Outline each uninfected red blood cell.
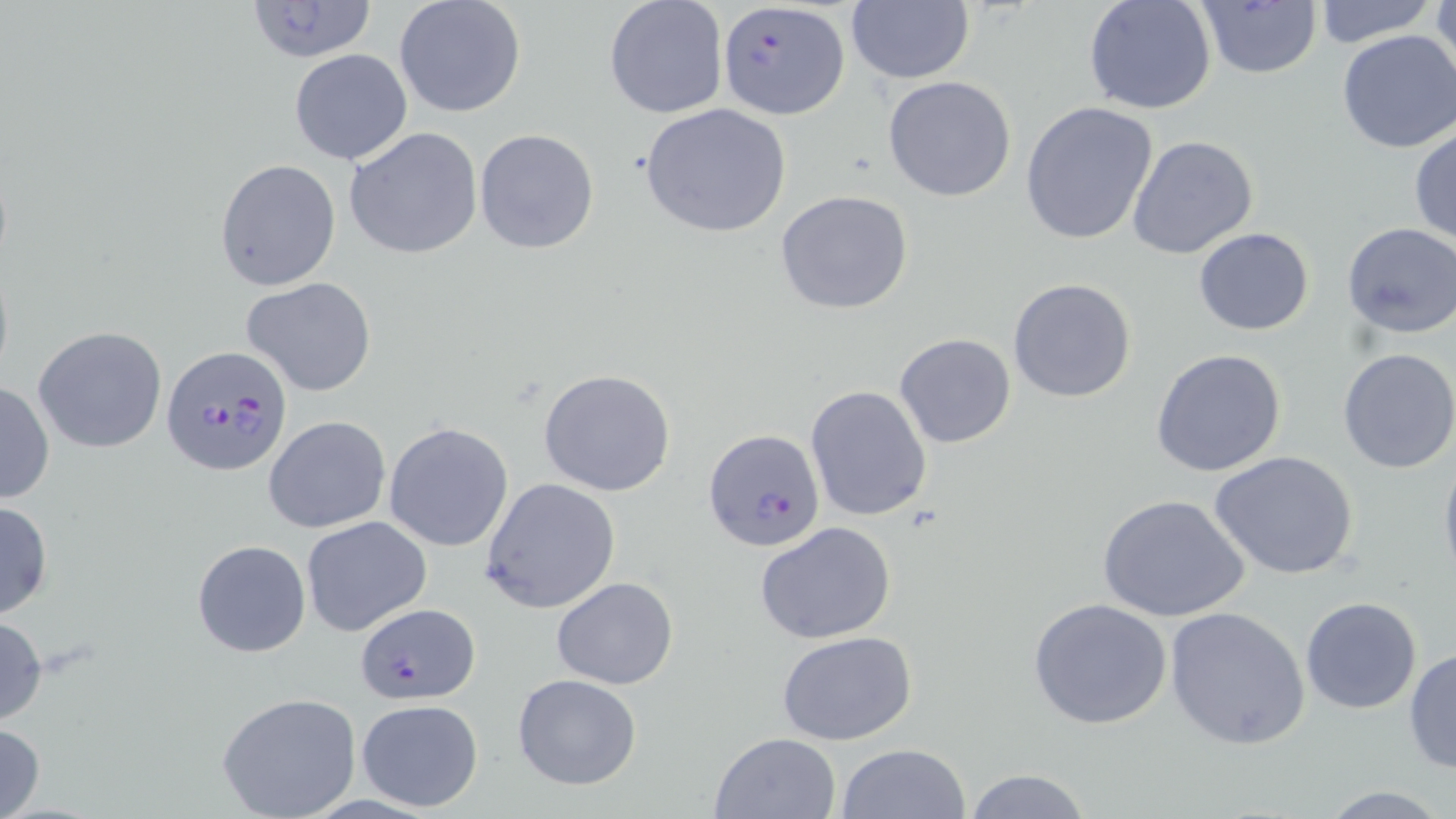
Approximate bounding boxes as (x1,y1)-(x2,y2) corner pairs in pixels.
Uninfected red blood cells: (393,0)-(527,120), (603,0)-(728,120), (846,0)-(974,86), (1083,0)-(1218,116), (1431,0)-(1456,87), (1312,1)-(1437,48), (1193,2)-(1323,80), (1335,29)-(1456,153), (289,48)-(413,165), (882,76)-(1016,203), (1020,101)-(1160,247), (639,104)-(791,237), (1409,122)-(1456,245), (344,126)-(482,260), (475,128)-(600,255), (1128,135)-(1259,259), (214,158)-(341,291), (774,189)-(915,315), (1339,222)-(1456,341), (1195,227)-(1315,336), (242,277)-(377,397), (1008,277)-(1137,403), (33,326)-(167,452), (894,333)-(1017,448), (1337,347)-(1456,473), (1151,348)-(1287,477), (537,369)-(677,496), (1,378)-(55,505), (804,384)-(932,523), (264,416)-(390,534), (384,422)-(513,552), (1439,448)-(1456,588), (1210,450)-(1360,580), (480,477)-(622,614), (1098,493)-(1251,624), (0,499)-(54,622), (301,515)-(432,636), (754,523)-(897,643), (191,539)-(311,659), (552,576)-(678,689), (1028,597)-(1174,730), (1300,597)-(1422,714), (1166,605)-(1311,748), (0,613)-(48,726), (775,630)-(920,746), (1405,647)-(1455,778), (511,673)-(642,790), (216,692)-(363,819), (356,698)-(484,813), (0,722)-(46,819), (709,731)-(841,818), (836,743)-(972,819), (962,769)-(1093,819), (1314,784)-(1452,818).

Summary:
  - Plasmodium falciparum-infected red blood cell locations: (241,0)-(381,65), (716,2)-(848,119), (162,345)-(294,479), (703,428)-(827,555), (354,607)-(477,707)
  - Slide-level diagnosis: Plasmodium falciparum
  - Stain: May-Grünwald-Giemsa
  - Preparation: thin blood film
  - Modality: light microscopy
  - Field of view: single
  - Image size: 1456×819 pixels
  - Magnification: 1000x